Name the blood parasite species.
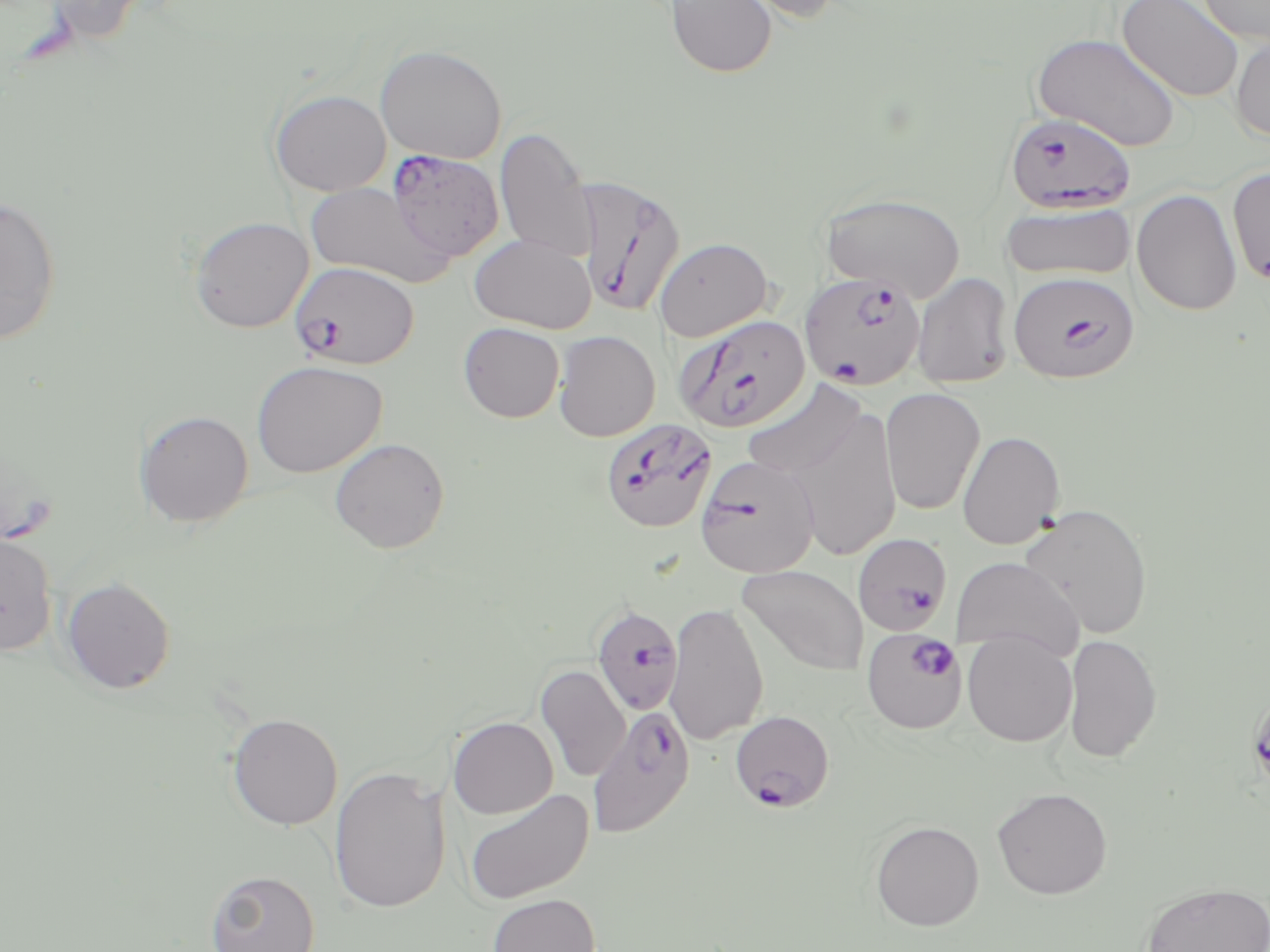

Plasmodium falciparum.

Approximate bounding boxes as named x1/y1/x2/y2 corners in pixels. Plasmodium falciparum-infected red blood cell locations: (x1=1004, y1=111, x2=1136, y2=213), (x1=388, y1=151, x2=503, y2=262), (x1=576, y1=176, x2=686, y2=316), (x1=288, y1=261, x2=419, y2=370), (x1=1008, y1=267, x2=1140, y2=382), (x1=800, y1=272, x2=925, y2=389), (x1=676, y1=315, x2=810, y2=432), (x1=600, y1=417, x2=715, y2=534), (x1=694, y1=455, x2=820, y2=578), (x1=854, y1=532, x2=954, y2=635), (x1=590, y1=604, x2=684, y2=716), (x1=862, y1=627, x2=968, y2=734), (x1=588, y1=704, x2=696, y2=839), (x1=729, y1=709, x2=835, y2=812). Uninfected red blood cell locations: (x1=38, y1=0, x2=156, y2=47), (x1=666, y1=0, x2=777, y2=77), (x1=732, y1=0, x2=845, y2=25), (x1=1117, y1=0, x2=1245, y2=102), (x1=1196, y1=0, x2=1270, y2=46), (x1=1229, y1=32, x2=1270, y2=143), (x1=1032, y1=33, x2=1182, y2=152), (x1=375, y1=44, x2=507, y2=163), (x1=270, y1=89, x2=391, y2=196), (x1=495, y1=127, x2=596, y2=263), (x1=1227, y1=166, x2=1270, y2=285), (x1=304, y1=182, x2=450, y2=287), (x1=1132, y1=189, x2=1242, y2=316), (x1=821, y1=192, x2=965, y2=302), (x1=0, y1=195, x2=62, y2=347), (x1=1001, y1=203, x2=1136, y2=281), (x1=189, y1=217, x2=313, y2=332), (x1=470, y1=233, x2=596, y2=333), (x1=654, y1=237, x2=773, y2=341), (x1=912, y1=273, x2=1014, y2=389), (x1=458, y1=322, x2=565, y2=422), (x1=554, y1=330, x2=660, y2=441), (x1=251, y1=360, x2=387, y2=478), (x1=742, y1=379, x2=867, y2=482), (x1=880, y1=386, x2=985, y2=515), (x1=787, y1=406, x2=902, y2=562), (x1=134, y1=410, x2=253, y2=527), (x1=957, y1=431, x2=1065, y2=549), (x1=330, y1=437, x2=450, y2=553), (x1=1019, y1=503, x2=1153, y2=640), (x1=0, y1=531, x2=58, y2=656), (x1=952, y1=557, x2=1084, y2=660), (x1=737, y1=566, x2=869, y2=676), (x1=61, y1=576, x2=176, y2=694), (x1=663, y1=601, x2=769, y2=745), (x1=962, y1=632, x2=1077, y2=746), (x1=1064, y1=633, x2=1162, y2=763), (x1=536, y1=664, x2=631, y2=782), (x1=227, y1=713, x2=343, y2=830), (x1=448, y1=716, x2=558, y2=818), (x1=330, y1=764, x2=450, y2=914), (x1=991, y1=787, x2=1113, y2=899), (x1=463, y1=788, x2=593, y2=905), (x1=870, y1=820, x2=985, y2=930), (x1=206, y1=869, x2=321, y2=952), (x1=1141, y1=882, x2=1270, y2=952), (x1=487, y1=893, x2=600, y2=952). Thin blood smear. 1000x magnification. One field of a larger specimen. May-Grünwald-Giemsa stain. Image is 1270×952 pixels. Light microscopy.